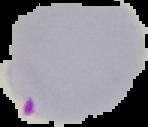 From a thin blood film. Malaria status: parasitized. Cell region segmented out of the field of view; the surrounding area is masked to black. Image is 148×127 pixels.